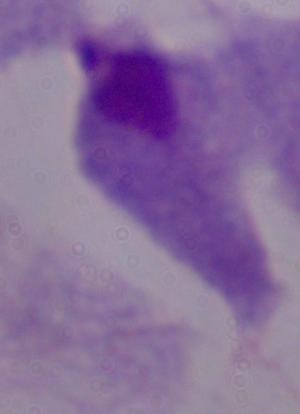

Captured at 1000x magnification. A trichomonad is seen. Photomicrograph.